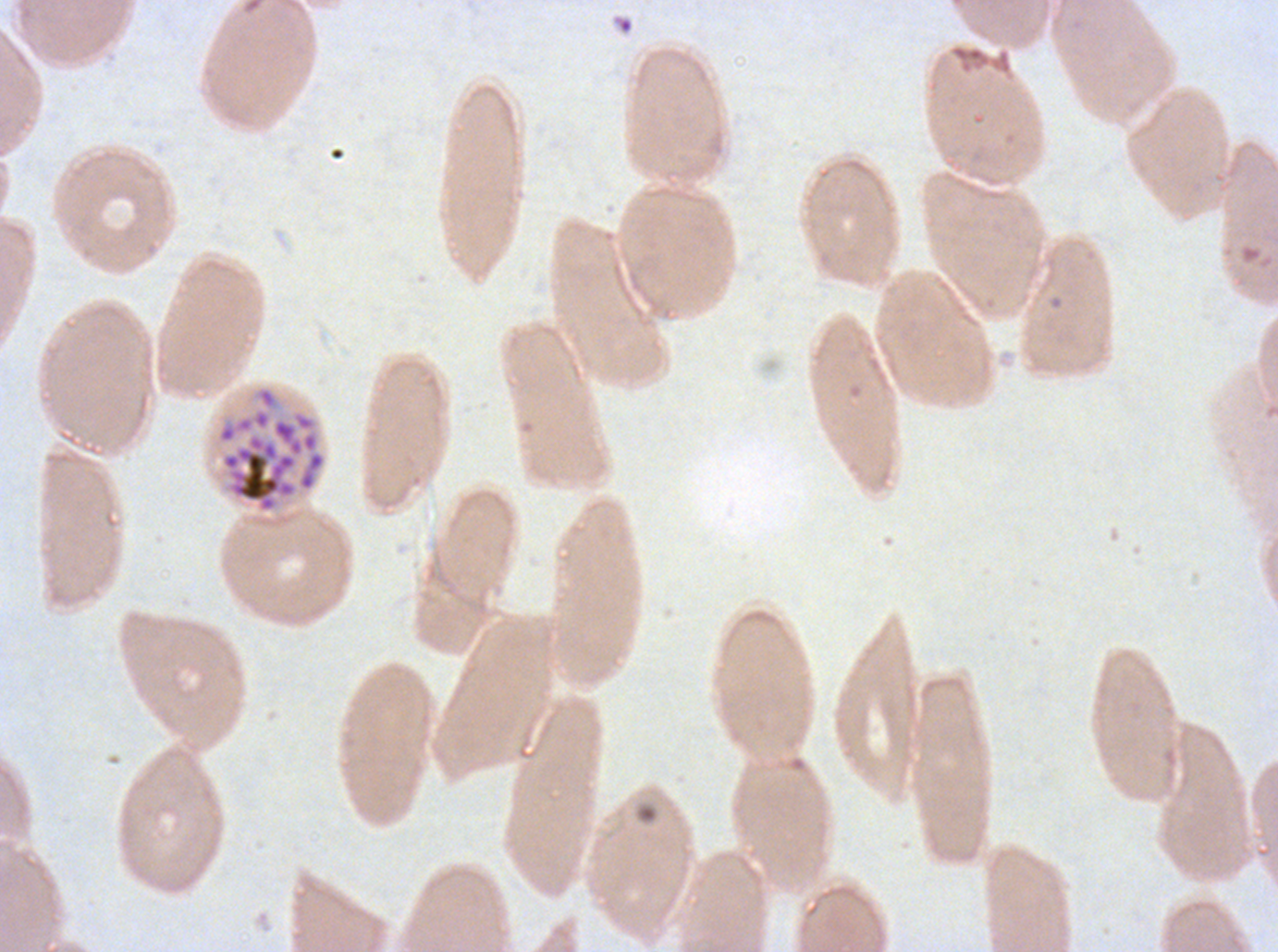
Approximate bounding boxes as (x1, y1, x2, y2) in pixels.
Summary:
  - Segmenter locations: (215, 384, 328, 515)
  - Debris locations: (616, 16, 634, 34)
  - Stain: Giemsa
  - Specimen: Plasmodium falciparum from a patient in The Gambia, cultured ex vivo for 24 to 48 hours
  - Field of view: one sub-image of a larger composite
  - Image size: 1278×952 pixels
  - Preparation: thin blood smear